Name the parasite shown.
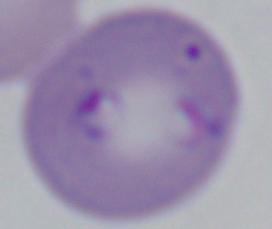
Babesia.

magnification: 1000x
modality: photomicrograph